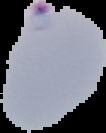
image type = cell region segmented out of the field of view; surrounding area masked to black
preparation = thin blood smear
result = Plasmodium parasites detected
image size = 106×133 pixels